Describe the morphology of the red blood cells.
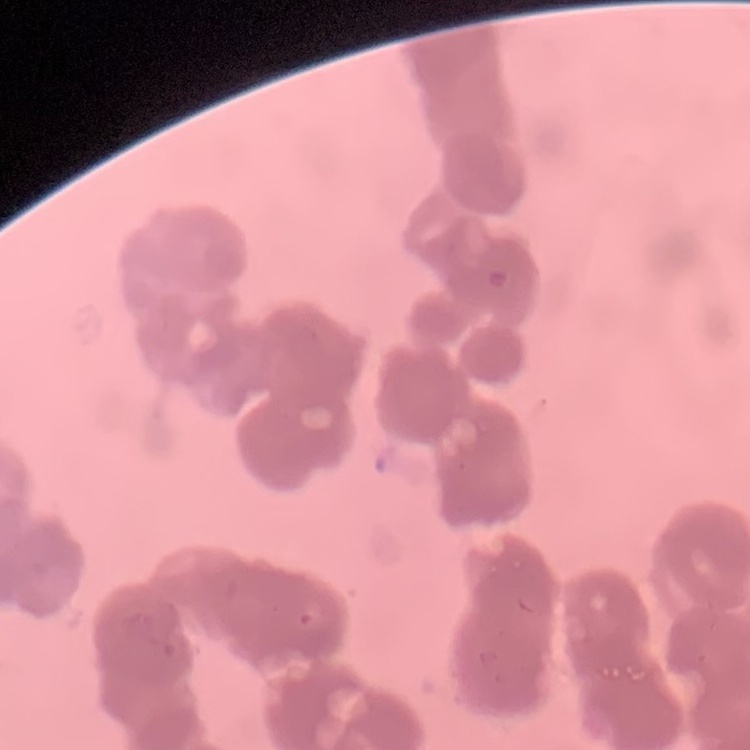
Rouleaux formation.

{
  "preparation": "thin blood smear",
  "image_type": "square crop of a larger photomicrograph",
  "stain": "Field's or Giemsa"
}